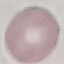
result = negative for malaria parasites
capture = smartphone camera at the microscope eyepiece
stain = Giemsa
preparation = thin blood film
image type = automatically extracted cell patch, resized to 64 × 64 pixels